Give the position of every Plasmodium parasite.
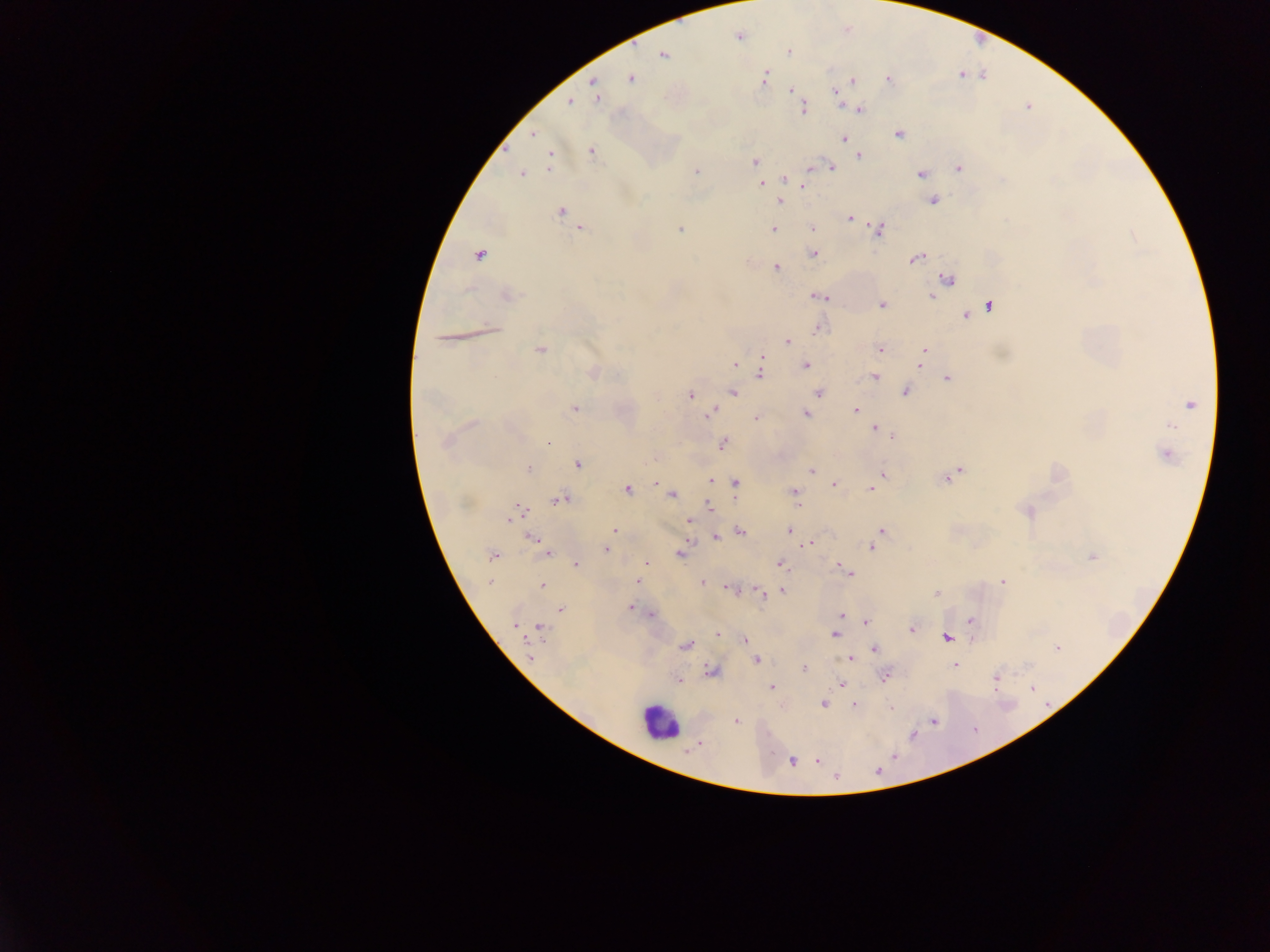
Approximate centers as {x, y} in pixels.
Plasmodium parasites: {738, 37}, {788, 51}, {663, 55}, {764, 78}, {631, 79}, {888, 80}, {852, 81}, {593, 82}, {790, 90}, {836, 92}, {596, 94}, {570, 102}, {804, 109}, {859, 110}, {533, 133}, {900, 134}, {844, 139}, {591, 151}, {859, 157}, {549, 159}, {755, 161}, {830, 166}, {959, 168}, {811, 169}, {696, 171}, {522, 173}, {921, 174}, {784, 179}, {761, 183}, {804, 185}, {780, 201}, {933, 201}, {560, 211}, {850, 218}, {581, 228}, {812, 228}, {681, 229}, {773, 229}, {878, 229}, {814, 254}, {479, 255}, {916, 258}, {776, 267}, {948, 278}, {507, 295}, {819, 296}, {932, 296}, {882, 305}, {989, 306}, {965, 316}, {818, 329}, {787, 341}, {880, 349}, {540, 350}, {924, 351}, {763, 359}, {736, 364}, {806, 365}, {919, 365}, {592, 372}, {760, 372}, {875, 376}, {948, 379}, {734, 392}, {819, 392}, {905, 392}, {691, 396}, {1190, 404}, {575, 408}, {855, 410}, {709, 414}, {806, 415}, {756, 417}, {877, 429}, {883, 432}, {890, 436}, {445, 442}, {547, 442}, {722, 444}, {1166, 454}, {578, 464}, {529, 468}, {811, 470}, {957, 472}, {884, 475}, {948, 478}, {710, 481}, {735, 483}, {833, 484}, {627, 489}, {871, 489}, {794, 492}, {671, 494}, {558, 500}, {796, 504}, {709, 506}, {519, 511}, {1027, 511}, {689, 520}, {614, 531}, {789, 531}, {740, 532}, {881, 532}, {717, 537}, {534, 539}, {810, 544}, {541, 546}, {872, 547}, {605, 548}, {548, 552}, {681, 553}, {492, 556}, {1092, 557}, {576, 564}, {647, 564}, {780, 564}, {846, 571}, {637, 581}, {1002, 581}, {490, 582}, {703, 583}, {542, 585}, {730, 588}, {783, 591}, {760, 592}, {937, 593}, {630, 608}, {560, 609}, {650, 615}, {842, 616}, {971, 620}, {866, 622}, {515, 625}, {540, 627}, {912, 629}, {717, 634}, {834, 635}, {947, 638}, {744, 639}, {685, 645}, {1057, 648}, {875, 649}, {529, 657}, {849, 658}, {757, 660}, {955, 665}, {804, 668}, {711, 671}, {885, 676}, {995, 679}, {678, 681}, {841, 684}, {772, 687}, {1032, 688}, {823, 704}, {854, 706}, {891, 708}, {737, 721}, {933, 721}, {700, 743}, {818, 760}, {792, 762}, {878, 770}, {836, 778}.

Leukocyte locations: {658, 722}. Thick blood smear. One field of view. Image is 1270×952 pixels. Sample from Ghana. Photographed through a microscope with a mobile-phone camera.